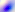
Summary:
  - Identification: Toxoplasma gondii
  - Magnification: 400x
  - Modality: photomicrograph